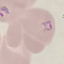

result = malaria parasites identified
preparation = thin blood film
stain = Giemsa
capture = smartphone through the microscope eyepiece
image type = automatically extracted cell patch, resized to 64 × 64 pixels